Classify this cell by malaria status.
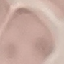

It is uninfected.

{
  "stain": "Giemsa",
  "image_type": "cell patch, automatically extracted from a larger field of view and resized to 64 × 64 pixels",
  "capture": "smartphone through the microscope eyepiece",
  "preparation": "thin smear"
}